Give the position of every Plasmodium parasite.
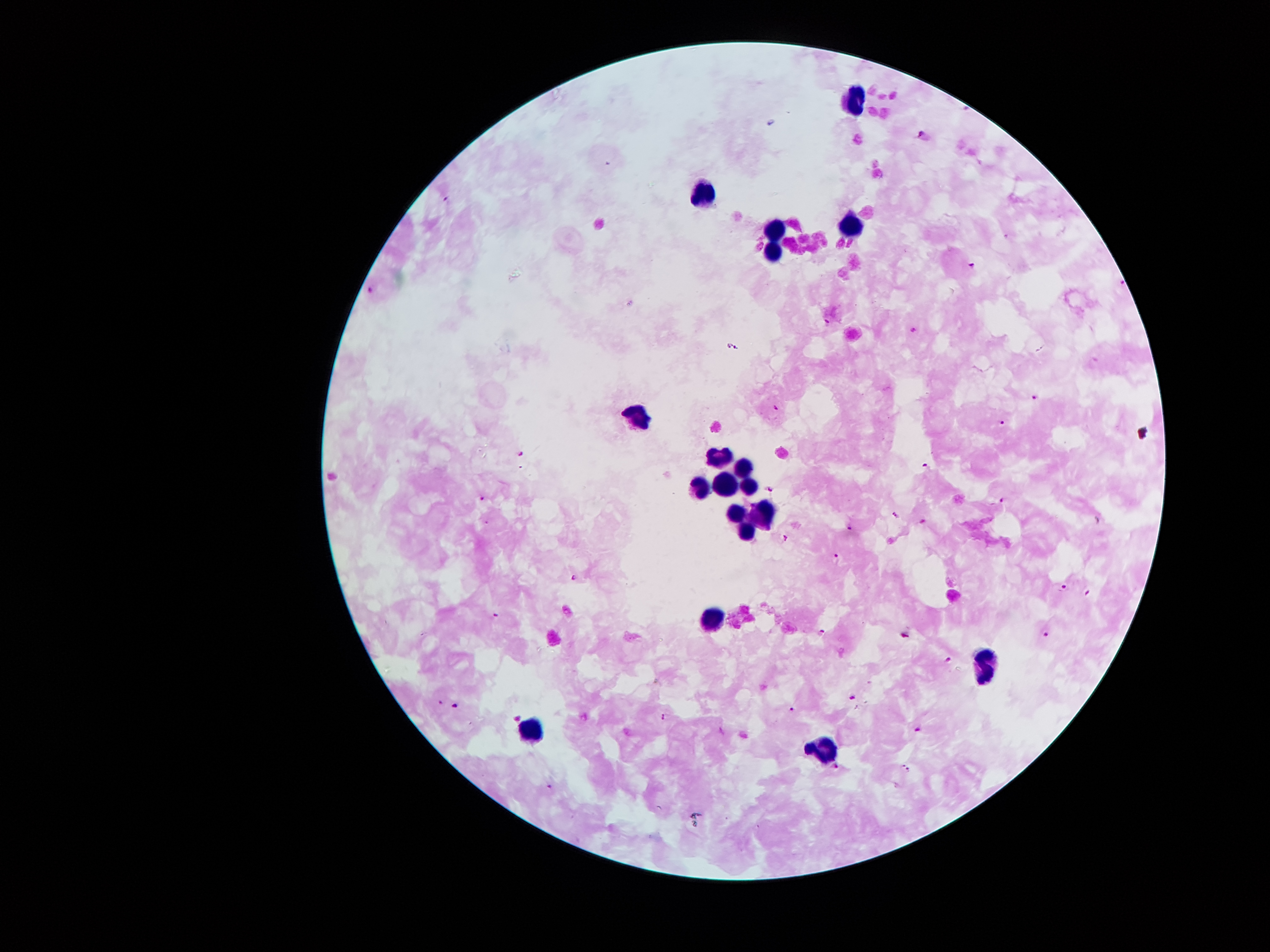

Approximate centers as (x, y) in pixels.
Plasmodium parasites: (923, 133), (446, 201), (973, 265), (371, 289), (827, 324), (913, 331), (733, 347), (1035, 400), (777, 409), (1004, 424), (524, 453), (926, 466), (772, 489), (483, 500), (1002, 501), (895, 516), (923, 520), (849, 526), (784, 539), (838, 554), (577, 576), (1064, 586), (1089, 592), (497, 615), (819, 631), (1047, 633), (904, 634), (948, 659), (853, 699), (438, 702), (456, 705), (791, 709), (665, 716), (918, 730), (904, 764), (835, 766), (909, 770), (549, 786).

capture: smartphone camera through the microscope eyepiece
magnification: 100x
patient_malaria_status: infected with Plasmodium falciparum
field_of_view: single
stain: Giemsa
image_size: 1270×952 pixels
preparation: thick peripheral-blood smear
leukocyte_locations: 'approximate centers as (x, y) in pixels: (857, 95), (702, 193), (849, 224), (776, 231), (770, 249), (639, 414), (717, 452), (745, 462), (720, 479), (695, 487), (748, 487), (735, 511), (763, 511), (744, 529), (710, 615), (985, 666), (529, 726), (824, 742)'